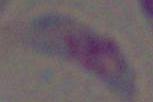
{
  "magnification": "1000x",
  "identification": "Toxoplasma gondii",
  "modality": "photomicrograph"
}